Give the extent of all Babesia divergens-infected red blood cells.
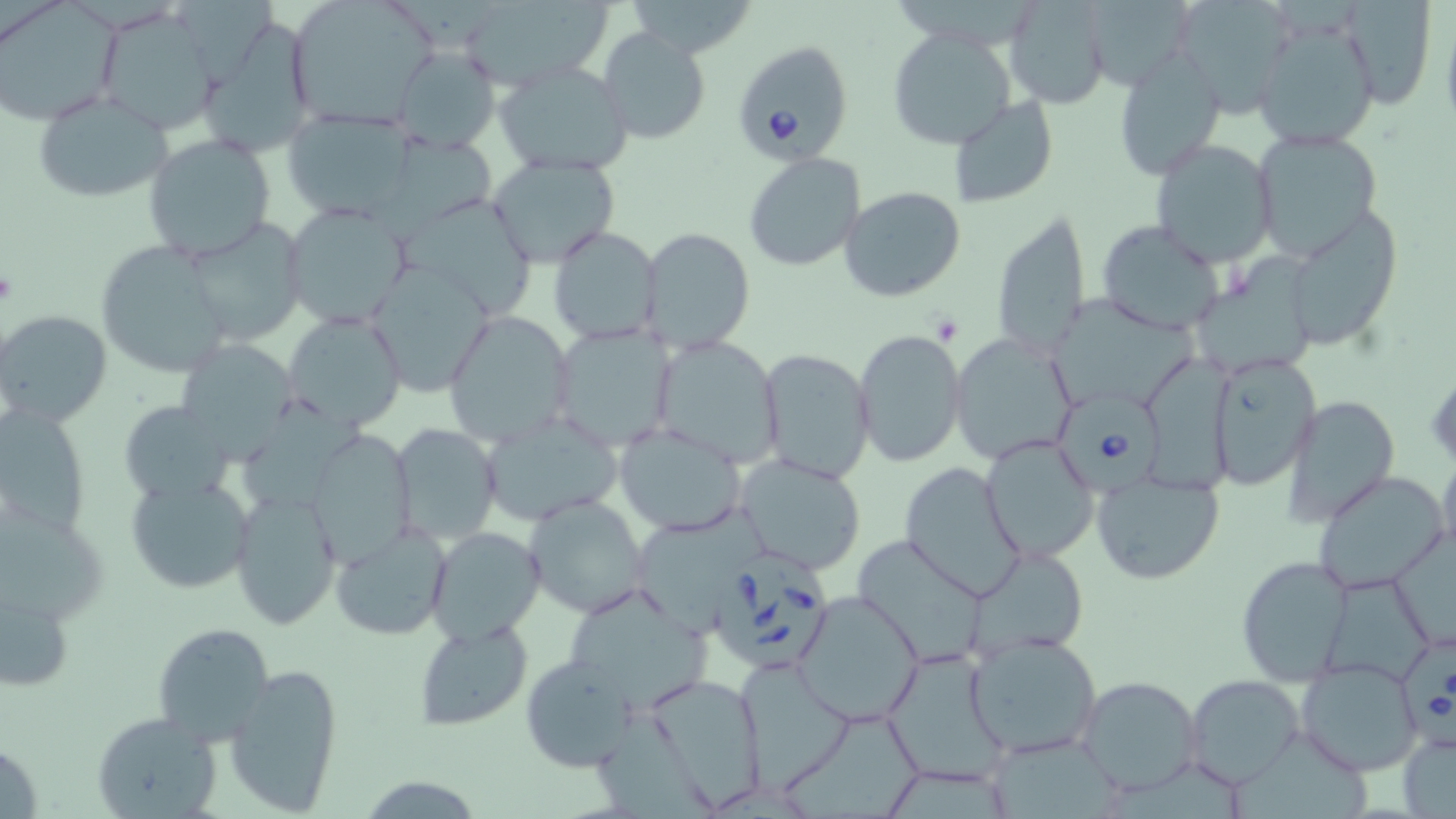

Approximate bounding boxes as (x1, y1, x2, y2) in pixels.
Babesia divergens-infected red blood cells: (732, 41, 853, 162), (1050, 392, 1166, 497), (714, 547, 839, 671), (1399, 636, 1456, 757).

Uninfected red blood cell locations: (286, 0, 438, 127), (1004, 0, 1112, 110), (1166, 0, 1298, 116), (1338, 0, 1440, 112), (0, 1, 123, 122), (458, 1, 614, 91), (1077, 2, 1192, 89), (94, 5, 225, 134), (1252, 18, 1381, 150), (203, 19, 318, 157), (886, 27, 1018, 151), (597, 28, 711, 146), (394, 45, 500, 153), (1114, 45, 1227, 180), (496, 61, 634, 178), (30, 88, 175, 203), (950, 95, 1058, 208), (281, 107, 414, 223), (1251, 129, 1384, 256), (143, 133, 277, 262), (1149, 138, 1278, 266), (742, 152, 867, 272), (484, 153, 624, 269), (839, 185, 967, 301), (398, 192, 541, 318), (281, 203, 413, 329), (1280, 205, 1401, 351), (991, 207, 1091, 359), (1096, 220, 1225, 335), (181, 221, 305, 346), (547, 225, 664, 347), (640, 227, 755, 350), (94, 240, 238, 381), (1187, 257, 1327, 375), (365, 261, 494, 397), (1056, 297, 1205, 407), (1, 310, 111, 426), (282, 310, 408, 430), (443, 310, 575, 448), (547, 323, 677, 450), (851, 326, 967, 471), (948, 333, 1079, 464), (651, 335, 783, 468), (177, 339, 298, 457), (757, 347, 875, 482), (1204, 352, 1321, 488), (1281, 394, 1401, 525), (118, 401, 233, 503), (0, 404, 92, 540), (478, 409, 627, 524), (390, 422, 502, 546), (614, 424, 747, 536), (304, 427, 415, 567), (980, 433, 1100, 563), (1437, 449, 1456, 561), (732, 452, 870, 575), (898, 460, 1025, 599), (1311, 471, 1452, 597), (1091, 472, 1224, 585), (125, 474, 256, 593), (229, 486, 341, 630), (522, 494, 650, 620), (0, 500, 107, 633), (633, 506, 775, 626), (330, 522, 452, 642), (427, 526, 544, 644), (852, 534, 993, 667), (973, 543, 1091, 656), (1236, 554, 1355, 688), (1319, 572, 1437, 688), (0, 584, 74, 696), (567, 588, 719, 712), (793, 588, 924, 728), (413, 620, 533, 732), (153, 623, 275, 746), (964, 630, 1105, 759), (882, 645, 1010, 789), (520, 655, 637, 772), (734, 656, 855, 787), (1295, 656, 1425, 776), (224, 661, 345, 816), (1076, 673, 1205, 795), (642, 674, 769, 806), (1185, 674, 1306, 786), (92, 711, 222, 819), (1396, 731, 1456, 818), (876, 760, 1018, 819). Slide-level diagnosis: Babesia divergens. Single field of view. Image is 1456×819 pixels. Captured at 1000x magnification. Optical microscopy. Thin blood film. May-Grünwald-Giemsa stain.